Report the malaria status of this cell.
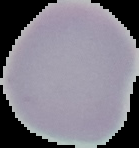
It is uninfected.

{
  "image_type": "segmented cell region with the area outside set to black",
  "image_size": "139×148 pixels",
  "preparation": "thin blood smear"
}